Give the extent of all uninfected red blood cells.
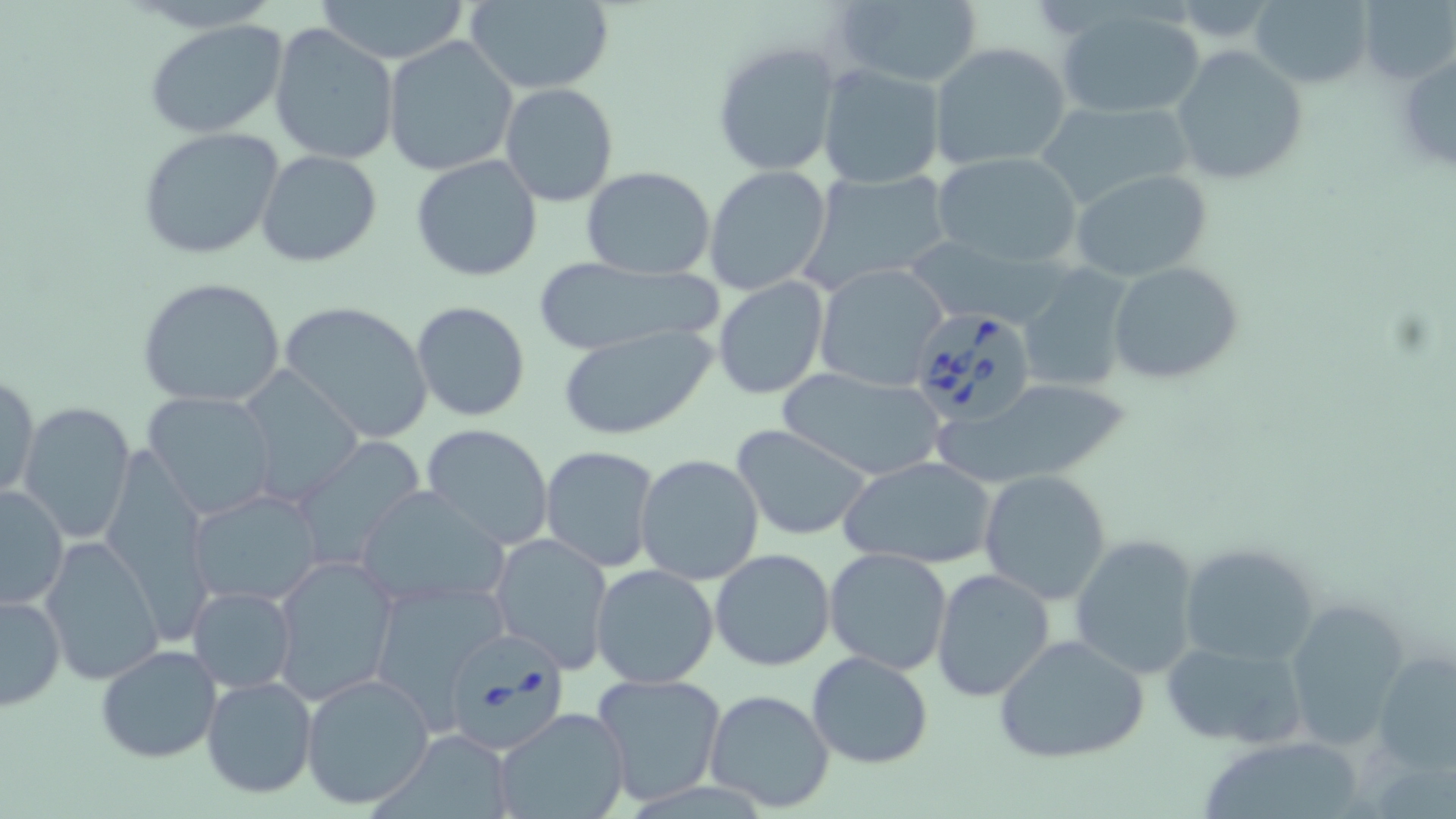
Approximate bounding boxes as [x1, y1, x2, y2] in pixels.
Uninfected red blood cells: [311, 0, 473, 65], [464, 0, 616, 94], [1250, 0, 1375, 88], [1356, 0, 1453, 85], [826, 1, 985, 88], [1053, 5, 1207, 121], [142, 18, 291, 139], [268, 22, 400, 166], [383, 36, 518, 177], [712, 38, 842, 176], [928, 41, 1076, 173], [1169, 46, 1309, 186], [1396, 48, 1456, 177], [818, 65, 946, 190], [499, 83, 618, 207], [1034, 99, 1195, 212], [136, 126, 286, 262], [256, 150, 383, 266], [931, 151, 1083, 269], [411, 155, 544, 283], [703, 164, 834, 296], [579, 166, 717, 279], [1069, 168, 1213, 282], [805, 169, 953, 291], [916, 241, 1080, 324], [525, 258, 727, 357], [1107, 261, 1245, 385], [814, 263, 951, 390], [1016, 265, 1136, 393], [713, 275, 830, 401], [136, 276, 287, 409], [278, 300, 435, 443], [410, 301, 531, 423], [555, 324, 717, 443], [776, 366, 946, 482], [237, 367, 365, 502], [1, 371, 41, 505], [950, 378, 1133, 487], [143, 391, 278, 518], [18, 400, 138, 545], [421, 422, 554, 550], [732, 424, 876, 542], [290, 438, 427, 570], [540, 446, 663, 573], [634, 452, 767, 585], [841, 455, 997, 570], [978, 469, 1113, 603], [0, 485, 69, 609], [353, 485, 510, 608], [187, 488, 327, 607], [489, 531, 615, 672], [1068, 534, 1203, 677], [40, 536, 166, 686], [1177, 541, 1321, 668], [824, 547, 954, 675], [710, 548, 836, 669], [271, 555, 399, 701], [589, 563, 721, 688], [931, 567, 1056, 701], [370, 577, 512, 717], [187, 585, 297, 694], [0, 593, 67, 710], [1284, 596, 1416, 746], [993, 634, 1149, 765], [1159, 635, 1310, 749], [95, 645, 223, 765], [1373, 649, 1456, 773], [805, 652, 934, 769], [593, 672, 726, 804], [300, 673, 436, 810], [201, 674, 319, 799], [704, 688, 836, 814], [494, 707, 630, 819], [1201, 744, 1366, 819].

Summary:
  - Babesia divergens-infected red blood cell locations: [906, 307, 1039, 428], [436, 623, 571, 757]
  - Slide-level diagnosis: Babesia divergens
  - Modality: optical microscopy
  - Magnification: 1000x
  - Preparation: thin blood film
  - Field of view: single
  - Image size: 1456×819 pixels
  - Stain: May-Grünwald-Giemsa